State which parasite is depicted.
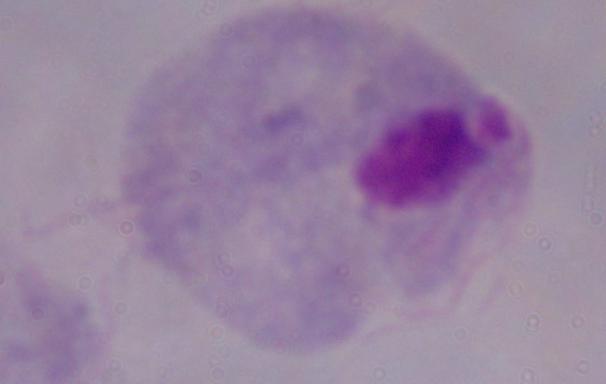
A trichomonad.

modality = micrograph
magnification = 1000x